Report the malaria status of this cell.
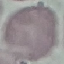

It is uninfected.

Summary:
  - Preparation: thin smear
  - Image type: automatically extracted cell patch, resized to 64 × 64 pixels
  - Capture: smartphone camera at the microscope eyepiece
  - Stain: Giemsa